Name the blood parasite species.
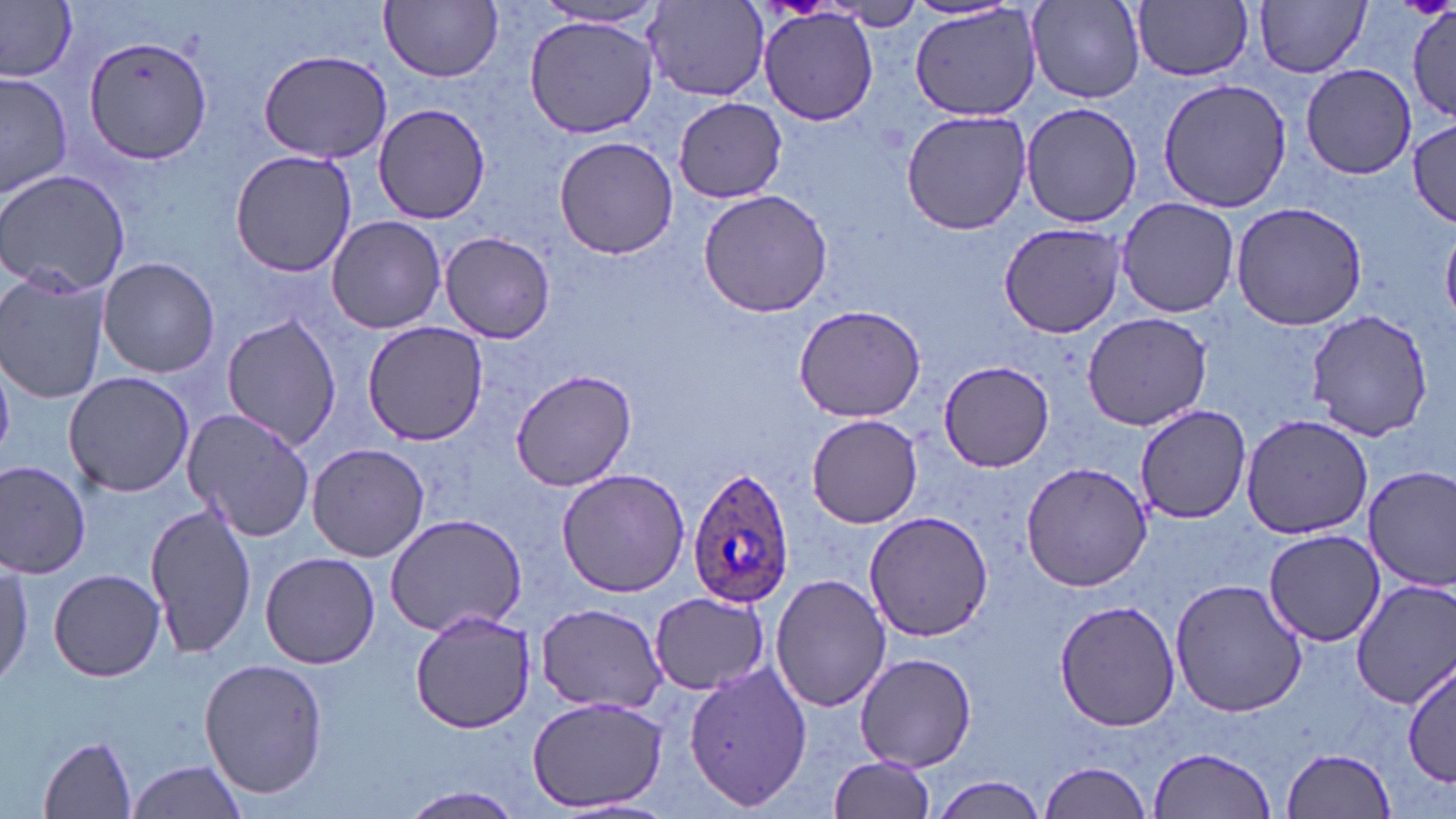
Plasmodium ovale.

Summary:
  - Coordinate format: approximate bounding boxes as (x1, y1, x2, y2) in pixels
  - Plasmodium ovale-infected red blood cell locations: (687, 465, 797, 608)
  - Uninfected red blood cell locations: (0, 0, 79, 80), (1132, 0, 1253, 81), (1256, 0, 1371, 79), (381, 1, 503, 82), (1028, 1, 1146, 103), (644, 2, 771, 100), (1406, 3, 1456, 121), (531, 4, 666, 30), (910, 5, 1041, 122), (758, 10, 879, 127), (524, 16, 660, 136), (83, 34, 214, 166), (256, 49, 397, 164), (1301, 64, 1416, 179), (1, 70, 72, 201), (1157, 77, 1292, 213), (674, 96, 786, 201), (1020, 101, 1142, 229), (373, 104, 491, 223), (901, 109, 1031, 235), (1408, 116, 1456, 227), (553, 134, 680, 259), (229, 150, 360, 277), (0, 169, 130, 294), (698, 189, 836, 317), (1115, 197, 1240, 317), (1229, 201, 1368, 330), (326, 215, 447, 334), (998, 221, 1127, 339), (440, 231, 556, 343), (96, 257, 221, 378), (0, 271, 112, 405), (793, 304, 928, 423), (1081, 311, 1212, 430), (1305, 312, 1433, 440), (221, 314, 342, 450), (362, 320, 487, 445), (937, 358, 1055, 472), (511, 368, 636, 491), (64, 371, 194, 498), (1133, 403, 1250, 526), (182, 409, 315, 541), (1240, 413, 1372, 537), (806, 414, 923, 528), (307, 443, 430, 563), (0, 459, 93, 579), (1020, 461, 1151, 591), (1364, 466, 1456, 591), (556, 468, 691, 597), (145, 501, 256, 660), (864, 510, 993, 643), (386, 513, 527, 637), (1263, 529, 1386, 645), (261, 552, 380, 669), (0, 554, 33, 687), (47, 567, 166, 682), (770, 572, 890, 712), (1352, 577, 1455, 709), (1170, 578, 1308, 718), (648, 592, 770, 692), (1054, 598, 1181, 732), (535, 604, 671, 712), (409, 610, 539, 733), (855, 652, 977, 769), (1405, 658, 1454, 788), (199, 659, 330, 798), (685, 662, 808, 811), (528, 695, 668, 813), (39, 735, 138, 816), (1148, 747, 1277, 818), (1282, 747, 1396, 818), (826, 756, 936, 819), (126, 758, 249, 819), (1038, 760, 1154, 819), (931, 776, 1051, 817), (390, 786, 533, 819)
  - Field of view: single
  - Preparation: thin blood film
  - Image size: 1456×819 pixels
  - Magnification: 1000x
  - Stain: May-Grünwald-Giemsa
  - Modality: light microscopy